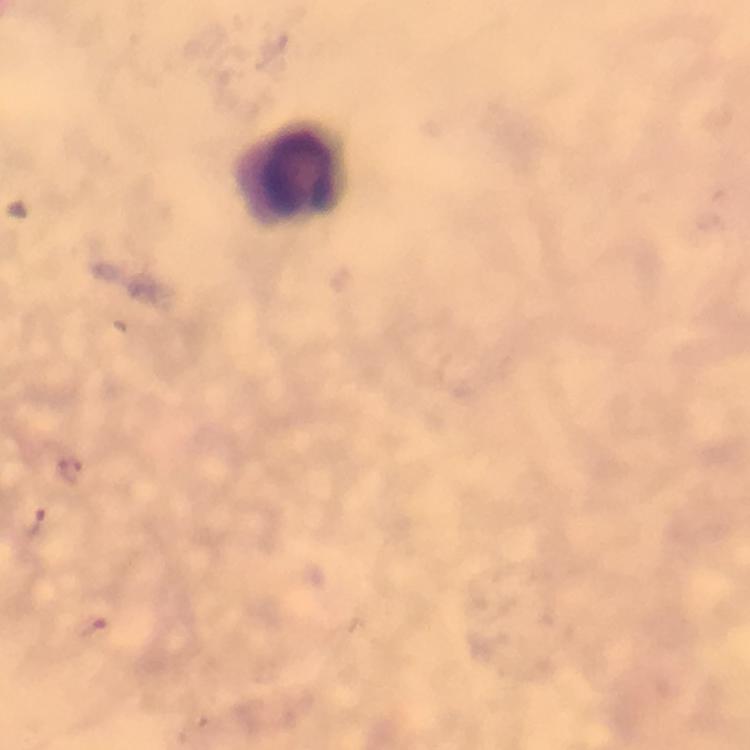
Approximate object centers, in pixels from the top-left corner.
Summary:
  - Leukocyte locations: (x=292, y=175)
  - Magnification: 100x
  - Image size: 750×750 pixels
  - Capture: smartphone camera through the microscope
  - Plasmodium parasites: none detected
  - Cropped from: a single field of view
  - Context: from a diagnostic examination for malaria
  - Immersion oil: applied
  - Preparation: thick blood smear
  - Stain: Giemsa